Report the malaria status of this cell.
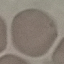

It is uninfected.

{
  "capture": "smartphone through the microscope eyepiece",
  "preparation": "thin blood film",
  "image_type": "cell patch, automatically extracted from a larger field of view and resized to 64 × 64 pixels",
  "stain": "Giemsa"
}